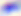
Summary:
  - Magnification: 400x
  - Modality: photomicrograph
  - Identification: Toxoplasma gondii